State the preparation type.
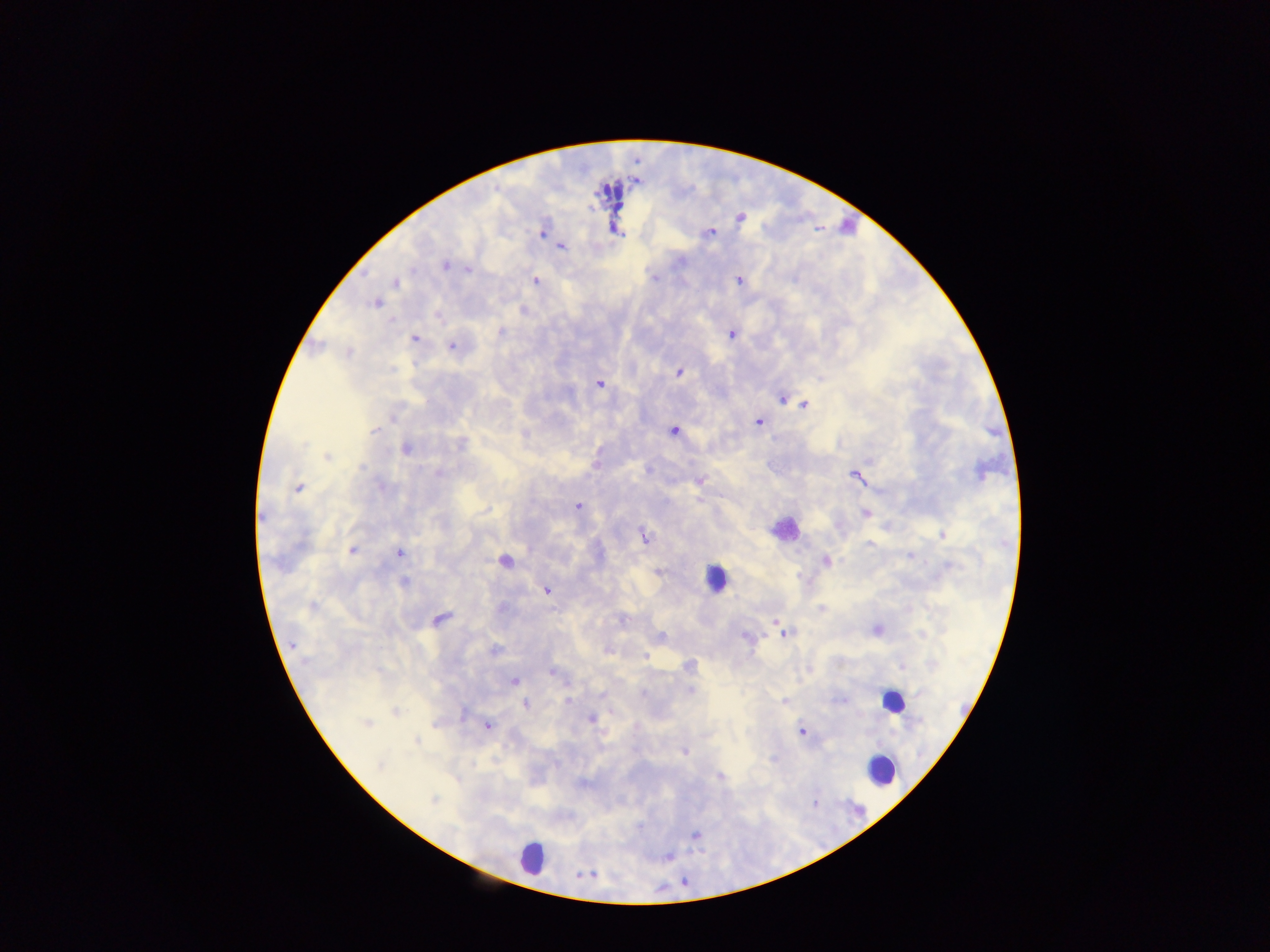
This is a thick smear.

Approximate centers as {x, y} in pixels.
Summary:
  - Malaria parasite locations: {739, 218}, {542, 232}, {711, 232}, {562, 247}, {447, 265}, {468, 267}, {535, 280}, {738, 280}, {398, 283}, {377, 302}, {438, 317}, {393, 321}, {502, 330}, {733, 334}, {417, 339}, {451, 345}, {393, 369}, {679, 372}, {599, 384}, {782, 400}, {807, 404}, {393, 417}, {758, 422}, {674, 429}, {374, 430}, {462, 443}, {407, 449}, {325, 455}, {646, 469}, {438, 472}, {856, 478}, {699, 482}, {298, 487}, {577, 505}, {485, 511}, {866, 513}, {943, 534}, {644, 535}, {872, 545}, {353, 550}, {400, 552}, {911, 556}, {827, 560}, {949, 564}, {660, 572}, {404, 581}, {547, 591}, {820, 608}, {773, 620}, {662, 634}, {747, 639}, {293, 647}, {493, 649}, {608, 652}, {645, 656}, {690, 665}, {903, 668}, {553, 672}, {515, 681}, {690, 690}, {568, 701}, {783, 701}, {527, 703}, {394, 712}, {462, 715}, {591, 718}, {368, 723}, {433, 724}, {486, 725}, {801, 732}, {417, 741}, {685, 752}, {380, 764}, {471, 765}, {719, 778}, {433, 801}, {695, 835}
  - Leukocyte locations: {783, 529}, {720, 576}, {891, 706}, {883, 774}, {527, 853}
  - Field of view: single
  - Image size: 1270×952 pixels
  - Capture: mobile-phone photograph through a microscope
  - Country: Ghana